Comment on the morphology of the red blood cells.
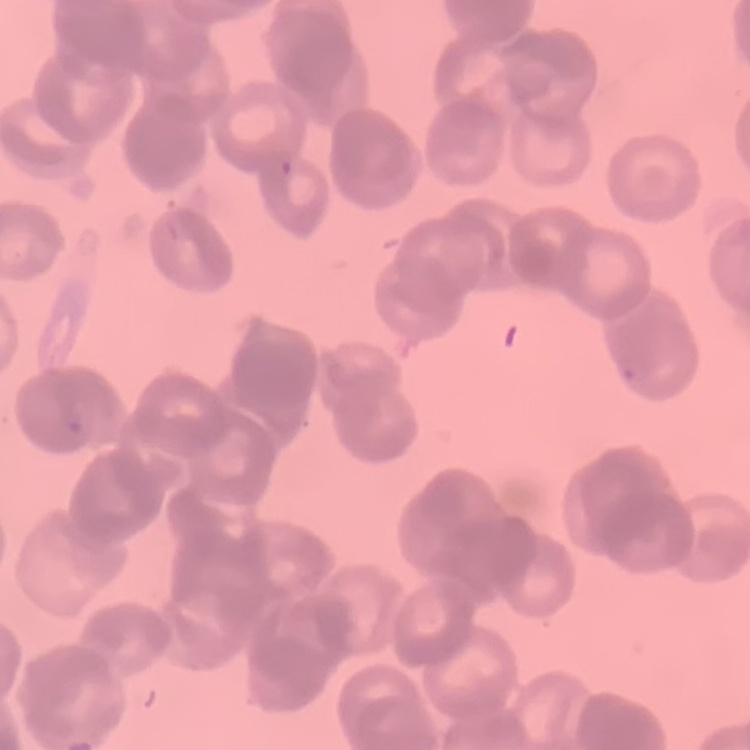
Rouleaux formation.

{
  "image_type": "one tile cut from a larger photomicrograph",
  "stain": "Field's or Giemsa",
  "preparation": "thin blood smear"
}